Point out malaria parasites and leukocytes.
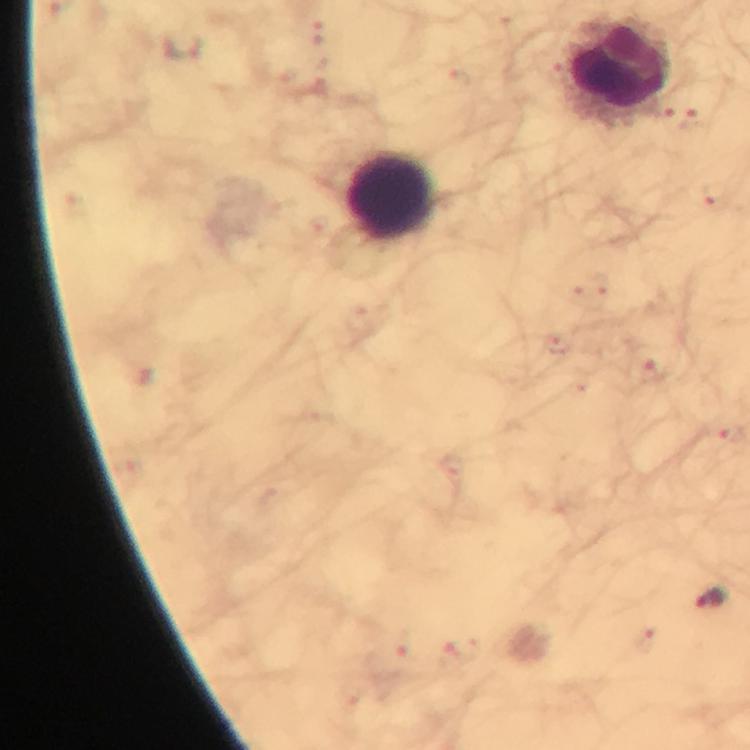

Approximate centers as (x, y) in pixels.
Malaria parasites: (714, 194), (652, 369), (711, 598).
Leukocytes: (618, 69), (391, 195).

image_size: 750×750 pixels
immersion_oil: applied
capture: smartphone camera through the microscope
preparation: thick blood film
stain: Giemsa
cropped_from: one field of view
magnification: 100x
context: from a diagnostic examination for malaria